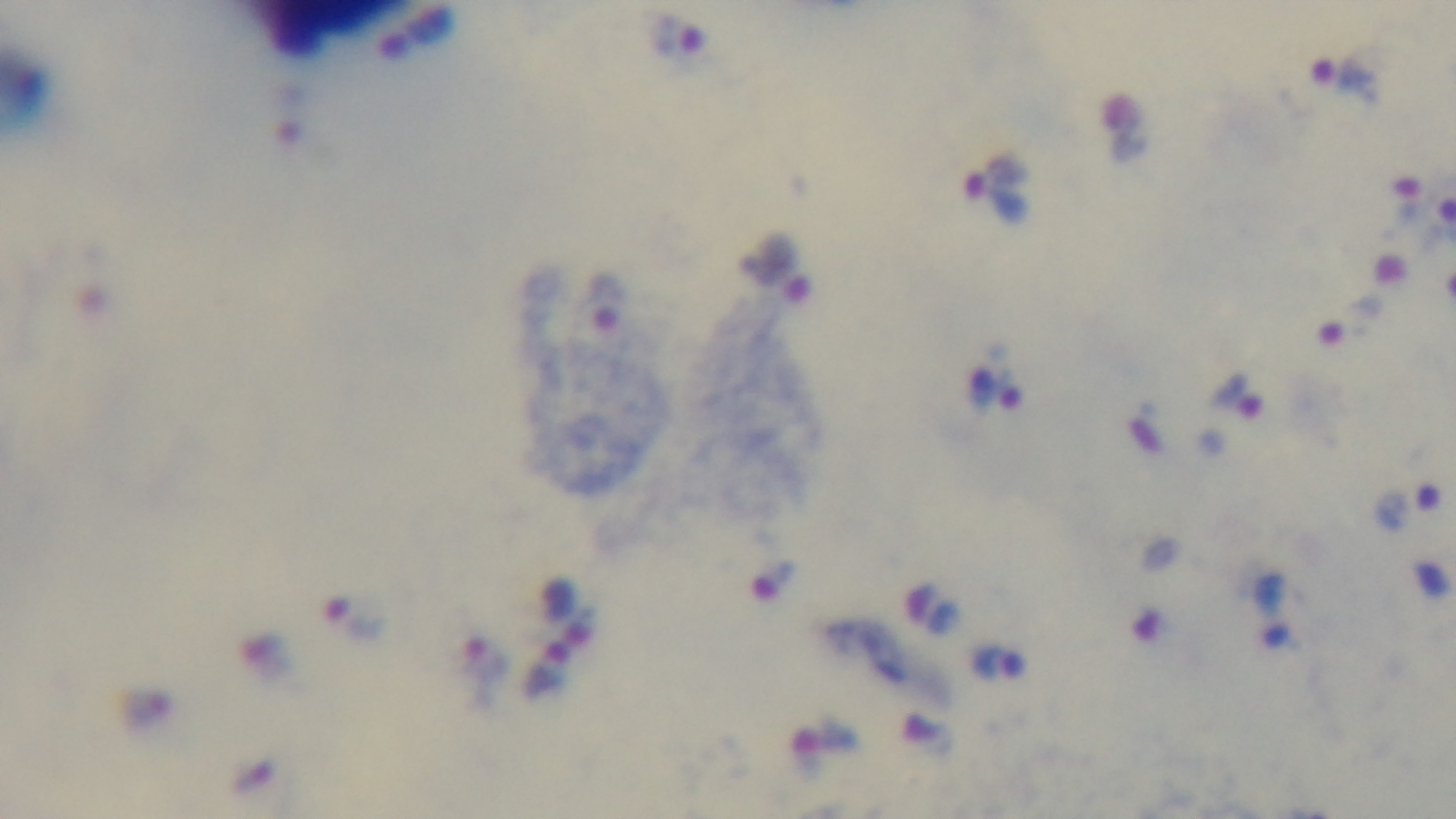

modality = light microscopy
preparation = thick blood film
stain = Giemsa
capture = mounted 4K digital camera
malaria status = positive
objective = 100x oil immersion
field of view = single